Locate the cells, classifying each as a parasitized red blood cell, an uninfected red blood cell, or a white blood cell.
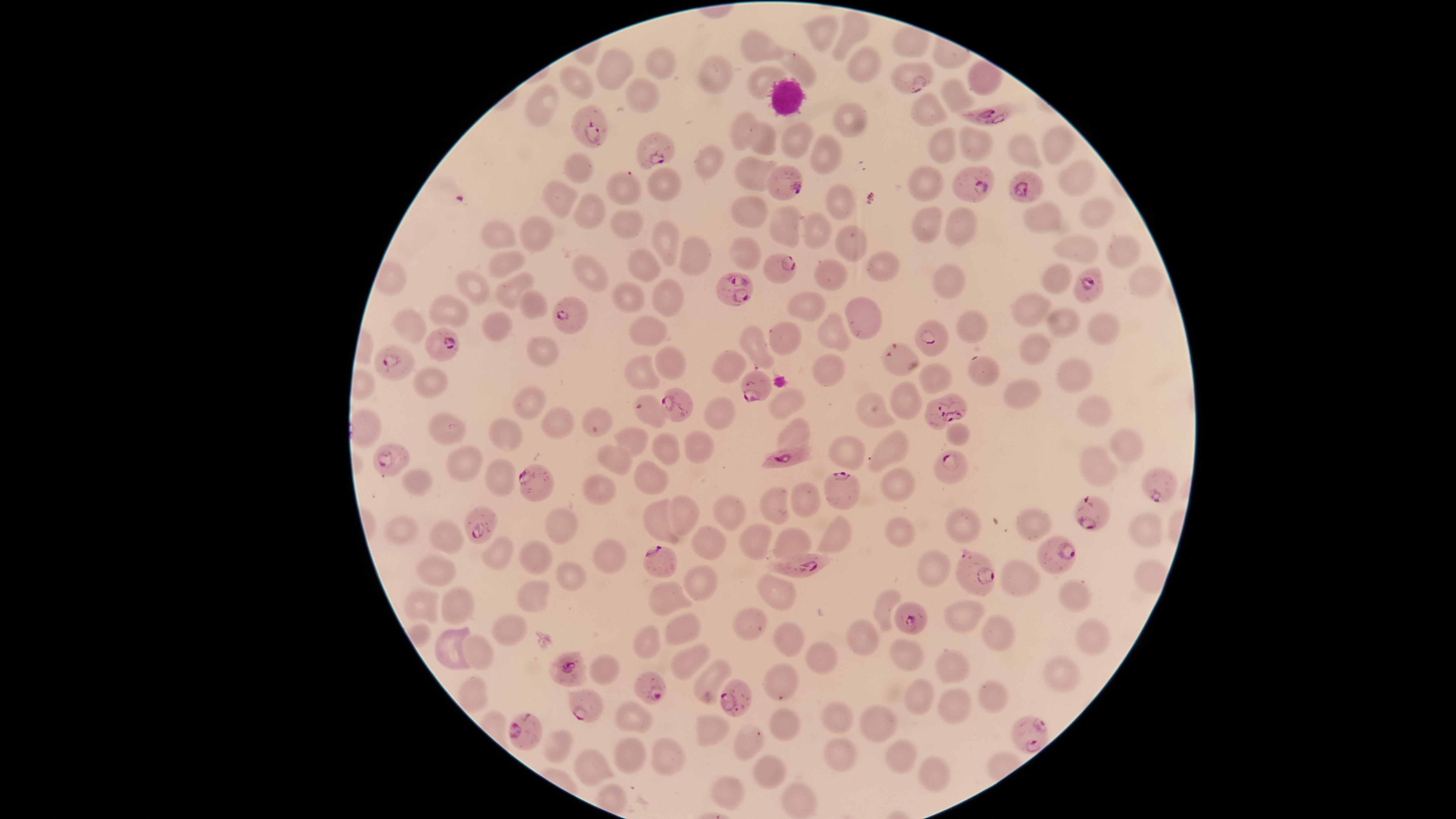

Approximate marker points as {x, y} in pixels.
Parasitized red blood cells: {912, 81}, {997, 114}, {592, 127}, {661, 149}, {783, 178}, {970, 187}, {1020, 190}, {779, 266}, {1086, 285}, {733, 291}, {566, 311}, {934, 335}, {447, 342}, {896, 356}, {395, 363}, {754, 394}, {675, 403}, {640, 408}, {942, 413}, {386, 454}, {792, 457}, {949, 465}, {1160, 481}, {843, 483}, {538, 485}, {1091, 515}, {484, 525}, {1055, 556}, {658, 563}, {800, 566}, {968, 572}, {913, 619}, {568, 667}, {650, 688}, {732, 697}, {588, 707}, {526, 732}, {1031, 734}.
Uninfected red blood cells: {852, 32}, {823, 36}, {757, 42}, {902, 43}, {663, 63}, {863, 65}, {798, 66}, {617, 67}, {712, 77}, {977, 80}, {571, 82}, {759, 85}, {956, 97}, {642, 98}, {544, 107}, {926, 110}, {850, 118}, {741, 127}, {796, 136}, {1052, 141}, {762, 144}, {976, 144}, {947, 149}, {823, 151}, {1024, 154}, {714, 165}, {577, 172}, {749, 172}, {1075, 176}, {663, 185}, {927, 188}, {623, 190}, {567, 200}, {838, 201}, {748, 210}, {1091, 211}, {586, 215}, {922, 222}, {1048, 223}, {632, 225}, {784, 226}, {815, 229}, {961, 232}, {497, 234}, {541, 235}, {670, 240}, {846, 242}, {1121, 248}, {1079, 251}, {747, 255}, {702, 258}, {504, 260}, {635, 262}, {876, 264}, {589, 272}, {946, 277}, {833, 278}, {1057, 280}, {1144, 281}, {475, 287}, {505, 287}, {665, 293}, {629, 297}, {532, 300}, {810, 307}, {1034, 309}, {455, 310}, {862, 310}, {1102, 324}, {976, 325}, {1060, 325}, {407, 326}, {496, 327}, {653, 331}, {785, 335}, {833, 335}, {1037, 342}, {541, 346}, {755, 351}, {670, 361}, {824, 364}, {730, 365}, {645, 369}, {978, 371}, {1076, 373}, {935, 379}, {426, 382}, {1024, 395}, {903, 401}, {532, 402}, {787, 404}, {718, 410}, {1091, 411}, {872, 412}, {595, 414}, {555, 423}, {795, 429}, {439, 432}, {960, 432}, {509, 434}, {629, 441}, {694, 445}, {1123, 445}, {843, 450}, {888, 450}, {669, 451}, {614, 461}, {462, 462}, {1096, 467}, {496, 476}, {653, 478}, {418, 480}, {895, 484}, {600, 489}, {805, 499}, {773, 506}, {687, 515}, {730, 515}, {1029, 519}, {558, 523}, {654, 523}, {963, 527}, {404, 531}, {896, 532}, {1146, 532}, {447, 534}, {840, 538}, {754, 539}, {794, 540}, {703, 542}, {501, 550}, {610, 553}, {539, 557}, {433, 568}, {934, 571}, {1009, 574}, {572, 577}, {695, 582}, {535, 593}, {774, 594}, {667, 595}, {1079, 595}, {883, 603}, {422, 606}, {456, 607}, {966, 617}, {683, 625}, {750, 625}, {513, 630}, {1091, 634}, {791, 635}, {996, 635}, {865, 639}, {451, 645}, {648, 645}, {477, 653}, {903, 653}, {686, 656}, {817, 659}, {605, 667}, {950, 671}, {1060, 673}, {703, 678}, {781, 684}, {468, 690}, {917, 696}, {996, 700}, {951, 707}, {632, 716}, {835, 717}, {709, 725}, {880, 725}, {786, 728}, {554, 743}, {746, 744}, {836, 751}, {899, 755}, {631, 756}, {668, 758}, {593, 763}, {768, 768}, {931, 772}, {727, 792}, {795, 795}.
No white blood cells identified.

Species: Plasmodium falciparum. The visible region is circular. Image is 1456×819 pixels. Giemsa stain. Photographed with a smartphone camera through the microscope eyepiece. One field of view of the specimen. Thin blood smear.